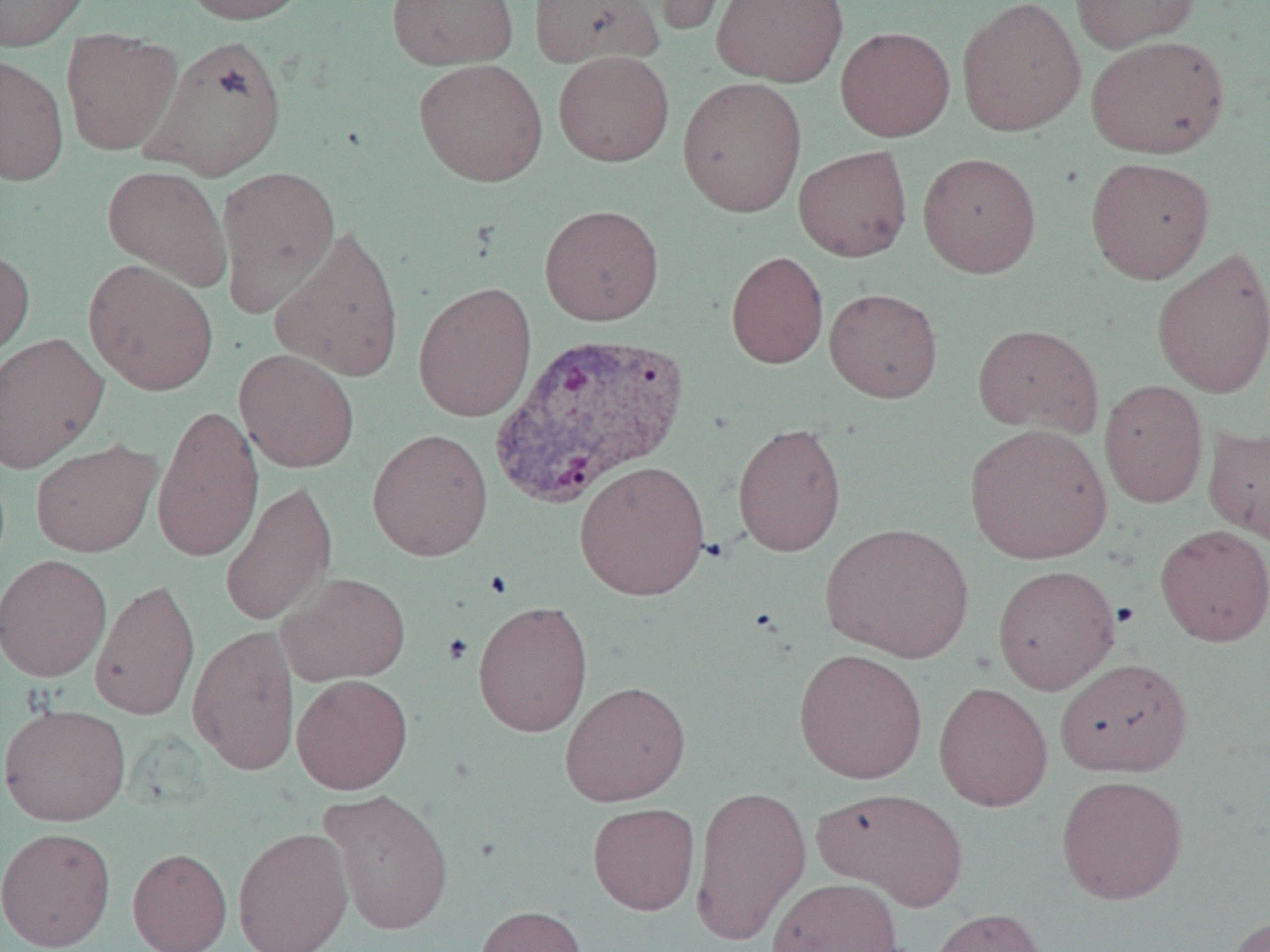

slide-level diagnosis = Plasmodium vivax
magnification = 1000x
uninfected red blood cell locations = approximate bounding boxes as named x1/y1/x2/y2 corners in pixels: (x1=0, y1=0, x2=92, y2=51), (x1=179, y1=0, x2=313, y2=25), (x1=386, y1=0, x2=518, y2=69), (x1=528, y1=0, x2=665, y2=69), (x1=645, y1=0, x2=740, y2=36), (x1=711, y1=0, x2=848, y2=87), (x1=956, y1=0, x2=1086, y2=137), (x1=1070, y1=0, x2=1201, y2=53), (x1=835, y1=26, x2=955, y2=141), (x1=60, y1=29, x2=183, y2=156), (x1=143, y1=34, x2=288, y2=180), (x1=1086, y1=35, x2=1229, y2=158), (x1=553, y1=50, x2=674, y2=167), (x1=0, y1=53, x2=69, y2=185), (x1=413, y1=58, x2=548, y2=187), (x1=677, y1=76, x2=807, y2=217), (x1=793, y1=145, x2=912, y2=262), (x1=918, y1=152, x2=1041, y2=278), (x1=1085, y1=156, x2=1215, y2=284), (x1=102, y1=165, x2=232, y2=291), (x1=216, y1=165, x2=340, y2=315), (x1=539, y1=204, x2=664, y2=325), (x1=270, y1=224, x2=405, y2=383), (x1=0, y1=246, x2=34, y2=366), (x1=1151, y1=247, x2=1270, y2=398), (x1=726, y1=251, x2=828, y2=369), (x1=83, y1=259, x2=219, y2=395), (x1=413, y1=281, x2=537, y2=422), (x1=824, y1=287, x2=943, y2=403), (x1=972, y1=323, x2=1104, y2=439), (x1=0, y1=332, x2=109, y2=473), (x1=234, y1=348, x2=360, y2=473), (x1=1099, y1=380, x2=1208, y2=508), (x1=152, y1=404, x2=264, y2=563), (x1=732, y1=422, x2=846, y2=556), (x1=964, y1=423, x2=1112, y2=564), (x1=1203, y1=424, x2=1270, y2=545), (x1=366, y1=428, x2=494, y2=561), (x1=31, y1=439, x2=161, y2=557), (x1=574, y1=460, x2=710, y2=601), (x1=219, y1=478, x2=337, y2=628), (x1=820, y1=522, x2=974, y2=663), (x1=1154, y1=524, x2=1270, y2=647), (x1=0, y1=554, x2=112, y2=683), (x1=993, y1=564, x2=1121, y2=695), (x1=277, y1=572, x2=412, y2=686), (x1=90, y1=577, x2=201, y2=721), (x1=472, y1=600, x2=593, y2=737), (x1=187, y1=626, x2=301, y2=776), (x1=794, y1=648, x2=928, y2=784), (x1=1055, y1=658, x2=1193, y2=777), (x1=291, y1=674, x2=413, y2=794), (x1=559, y1=680, x2=691, y2=807), (x1=933, y1=681, x2=1053, y2=811), (x1=0, y1=702, x2=131, y2=826), (x1=1056, y1=774, x2=1188, y2=905), (x1=689, y1=785, x2=811, y2=946), (x1=814, y1=786, x2=968, y2=910), (x1=318, y1=788, x2=454, y2=934), (x1=588, y1=803, x2=700, y2=915), (x1=0, y1=826, x2=116, y2=951), (x1=232, y1=826, x2=354, y2=952), (x1=128, y1=847, x2=232, y2=952), (x1=767, y1=877, x2=903, y2=952), (x1=475, y1=905, x2=588, y2=952), (x1=927, y1=907, x2=1049, y2=952), (x1=1220, y1=914, x2=1270, y2=952)
modality = light microscopy
Plasmodium vivax-infected red blood cell locations = approximate bounding boxes as named x1/y1/x2/y2 corners in pixels: (x1=490, y1=329, x2=690, y2=509)
image size = 1270×952 pixels
field of view = single
preparation = thin blood smear